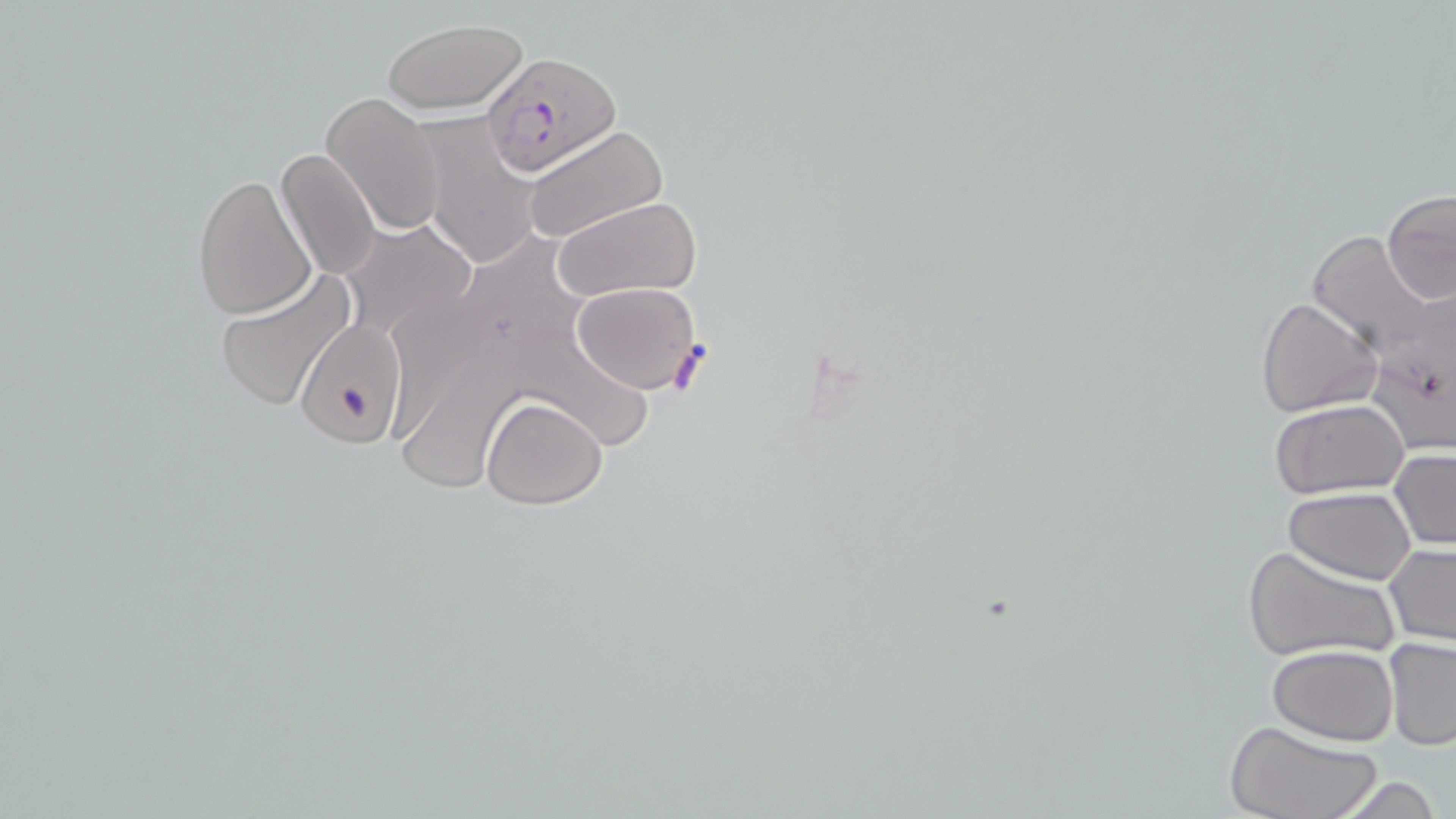

Summary:
  - Coordinate format: approximate bounding boxes as (x1, y1, x2, y2) in pixels
  - Uninfected red blood cell locations: (382, 17, 528, 115), (321, 92, 446, 235), (415, 118, 544, 268), (520, 125, 671, 246), (276, 146, 381, 283), (191, 171, 318, 322), (1380, 189, 1456, 309), (552, 196, 702, 303), (338, 219, 480, 346), (1306, 230, 1438, 358), (211, 270, 358, 414), (569, 280, 704, 393), (383, 281, 509, 449), (1366, 286, 1456, 456), (1256, 296, 1381, 418), (296, 321, 409, 449), (525, 330, 665, 450), (409, 358, 515, 495), (481, 395, 607, 510), (1269, 401, 1410, 499), (1389, 448, 1455, 551), (1284, 486, 1417, 584), (1240, 544, 1398, 664), (1385, 544, 1455, 647), (1383, 636, 1456, 750), (1266, 643, 1398, 745), (1224, 718, 1381, 819)
  - Plasmodium falciparum-infected red blood cell locations: (480, 49, 621, 179)
  - Slide-level diagnosis: Plasmodium falciparum
  - Image size: 1456×819 pixels
  - Stain: May-Grünwald-Giemsa
  - Modality: light microscopy
  - Magnification: 1000x
  - Preparation: thin blood film
  - Field of view: one of a larger specimen